Identify the cell.
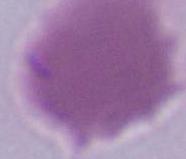
This is an erythrocyte.

Summary:
  - Magnification: 1000x
  - Modality: photomicrograph